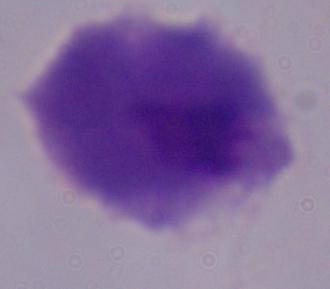

identification: trichomonad
modality: micrograph
magnification: 1000x